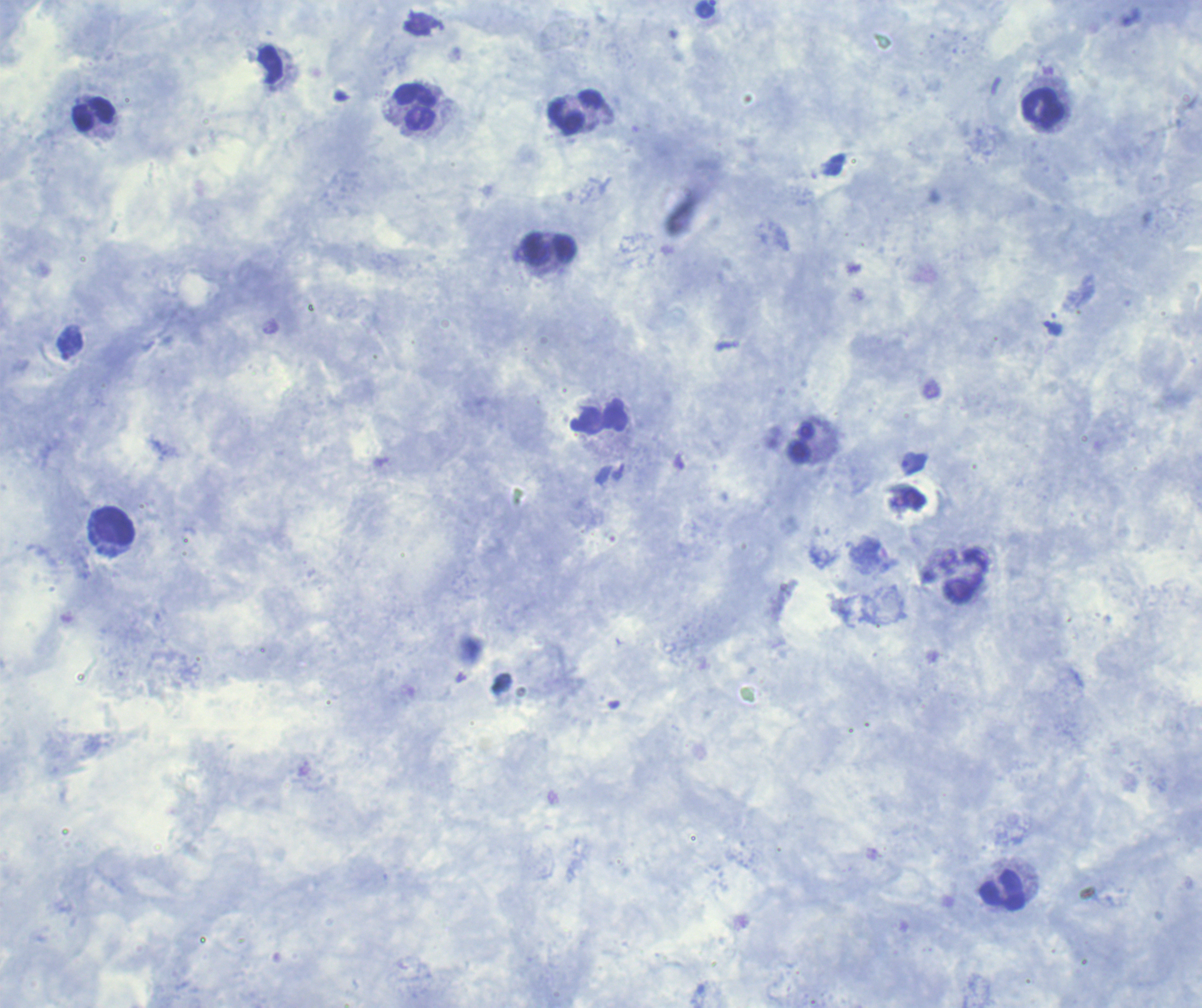

Approximate centers as (x, y) in pixels.
Summary:
  - Leukocyte locations: (415, 107), (1043, 108), (576, 112), (94, 114), (549, 249), (599, 417), (115, 525), (1003, 890)
  - Trophozoite locations: (706, 9), (421, 24), (1053, 329), (914, 464)
  - Stain: Romanowsky
  - Background quality: good
  - Result: positive for Plasmodium parasites
  - Magnification: 100x
  - Field of view: single
  - Preparation: thick smear of blood
  - Image size: 1202×1008 pixels
  - Coloration quality: good
  - Context: previously used in a real diagnosis